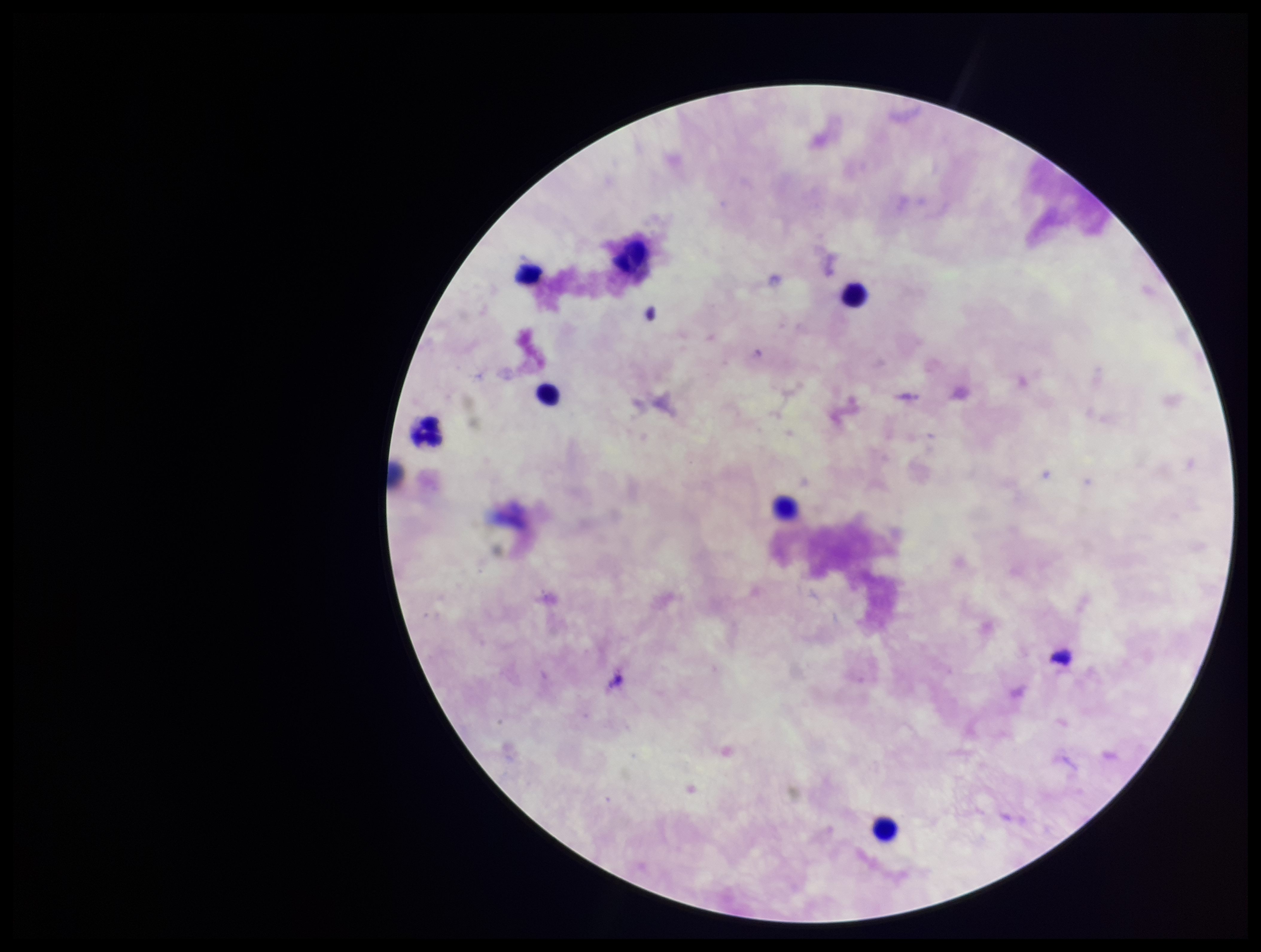
{
  "parasite_count": 0,
  "plasmodium_parasites": "none detected",
  "preparation": "thick blood smear",
  "field_of_view": "single",
  "leukocyte_count": 8,
  "stain": "Giemsa",
  "capture": "smartphone photograph through the microscope eyepiece",
  "image_size": "1261×952 pixels",
  "patient_malaria_status": "negative"
}